Point out each malaria parasite.
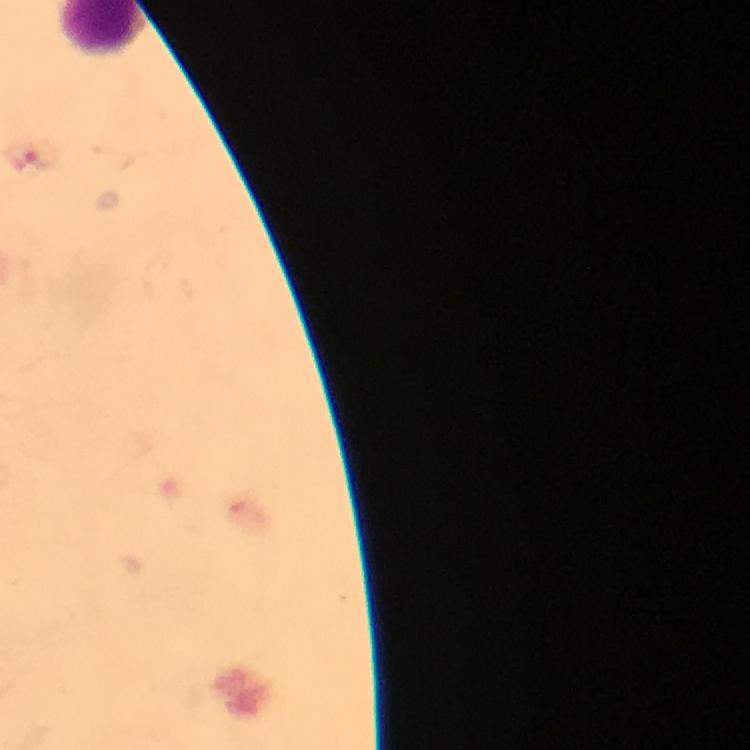

Approximate centers as [x, y] in pixels.
Malaria parasites: [26, 156].

Summary:
  - Cropped from: a single field of view
  - Magnification: 100x
  - Preparation: thick blood smear
  - Context: from a malaria diagnostic workup
  - Immersion oil: applied
  - Image size: 750×750 pixels
  - Capture: smartphone photograph through a microscope
  - Stain: Giemsa